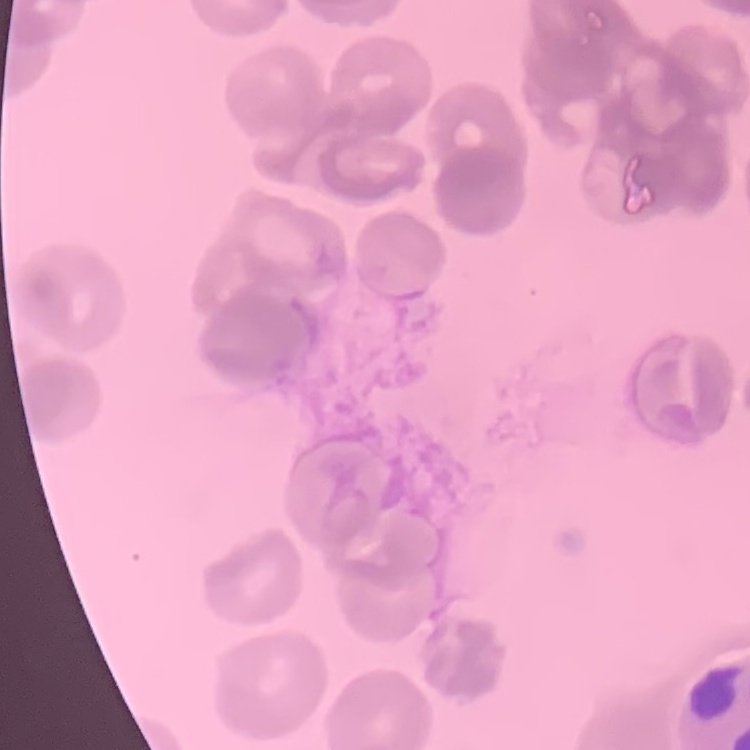
Summary:
  - Erythrocyte morphology: rouleaux formation
  - Stain: Field's or Giemsa
  - Image type: square crop of a larger photomicrograph
  - Preparation: thin blood smear